Report the malaria status of this cell.
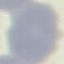
Uninfected.

stain = Giemsa
preparation = thin blood smear
image type = cell patch, automatically extracted from a larger field of view and resized to 64 × 64 pixels
capture = smartphone through the microscope eyepiece